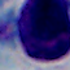 A white blood cell is shown. 1000x magnification. Micrograph.